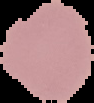
{
  "malaria_status": "uninfected",
  "image_type": "cell region segmented out of the field of view; surrounding area masked to black",
  "image_size": "94×103 pixels",
  "preparation": "thin blood film"
}